Give the position of every Plasmodium parasite visible.
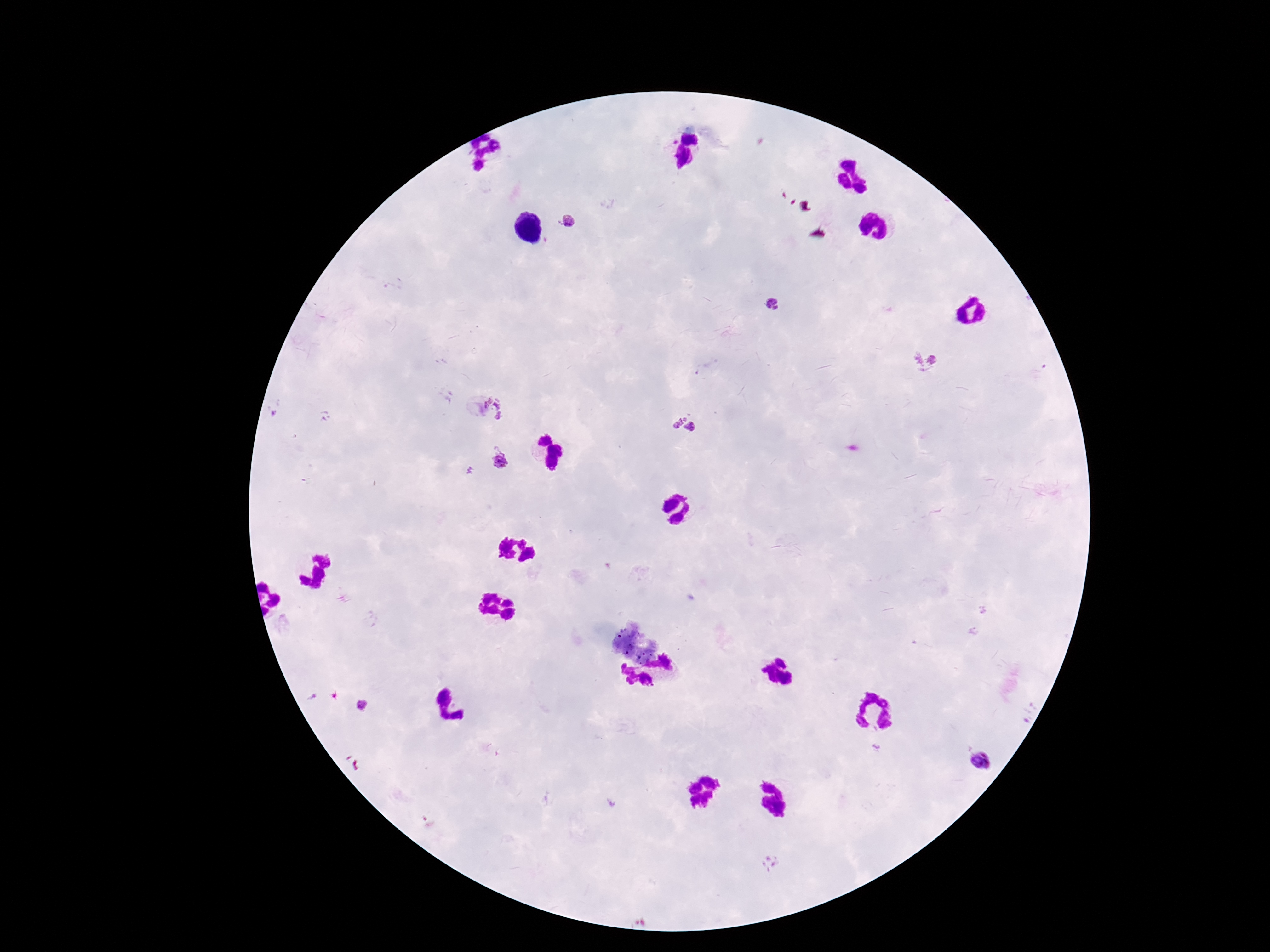
Approximate object centers, in pixels from the top-left corner.
Plasmodium parasites: (x=568, y=222), (x=773, y=306), (x=924, y=361), (x=496, y=408), (x=683, y=426), (x=500, y=463), (x=362, y=705), (x=982, y=761).

One field from this slide. Photographed through the microscope eyepiece with a smartphone camera. Thick blood film. Image is 1270×952 pixels. Giemsa stain. Patient malaria status: infected. 100x magnification.